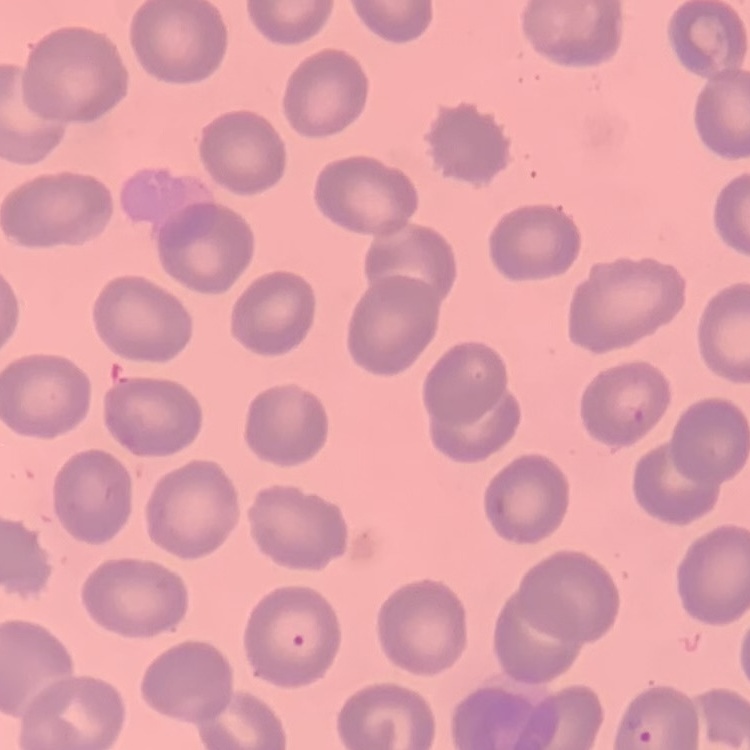

red blood cell morphology = no rouleaux formation
preparation = thin peripheral smear
stain = Field's or Giemsa
image type = one tile cut from a larger photomicrograph